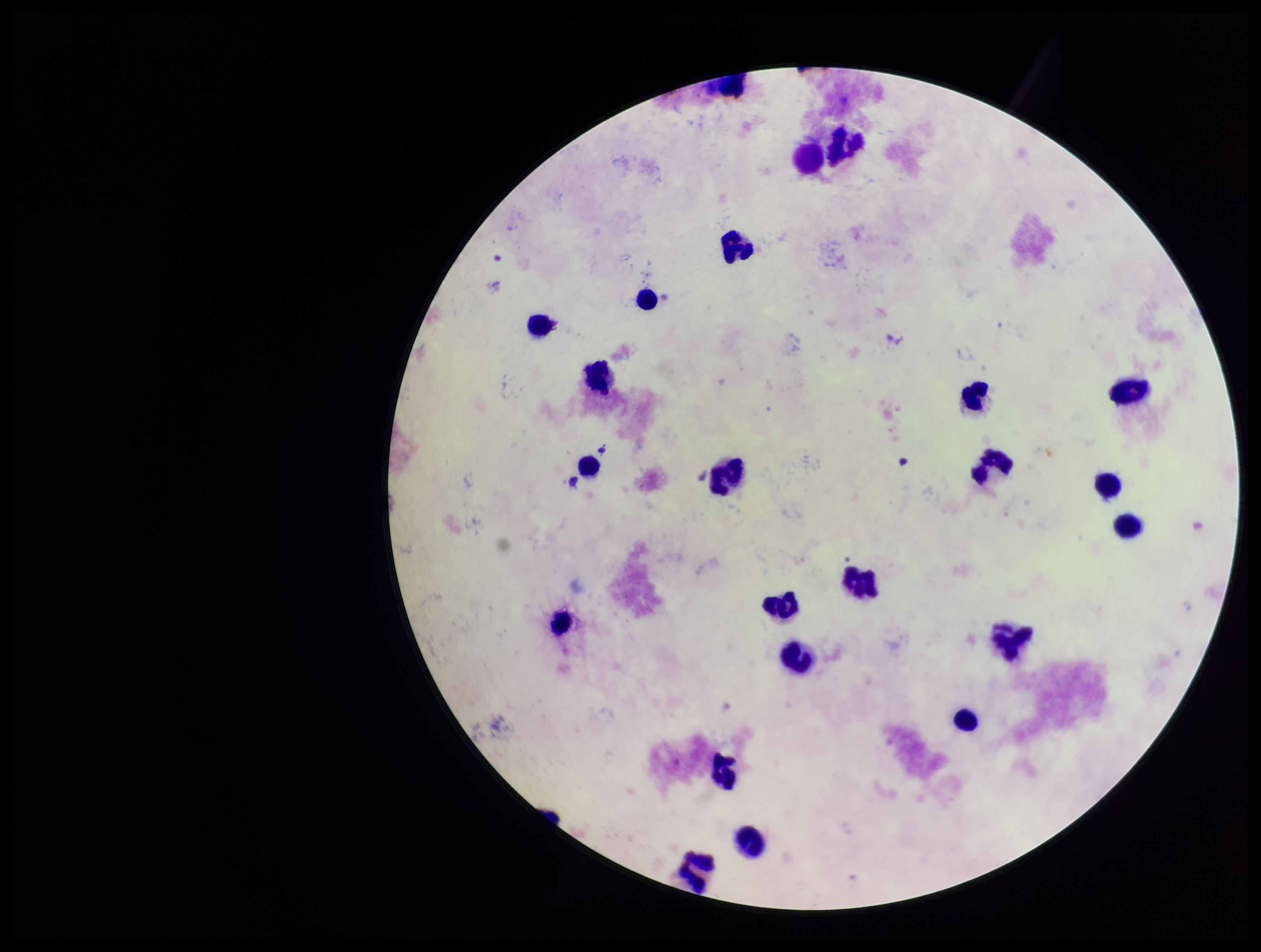 Giemsa stain. Parasite count: 0. Patient malaria status: negative. Image is 1261×952 pixels. Leukocyte count: 23. Single field of view. Photographed through the microscope eyepiece with a smartphone camera. Preparation: thick smear. Plasmodium parasites: none seen.